Classify this cell by malaria status.
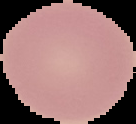
It is uninfected.

{
  "preparation": "thin blood film",
  "image_size": "136×124 pixels",
  "image_type": "cell region segmented out of the field of view; surrounding area masked to black"
}